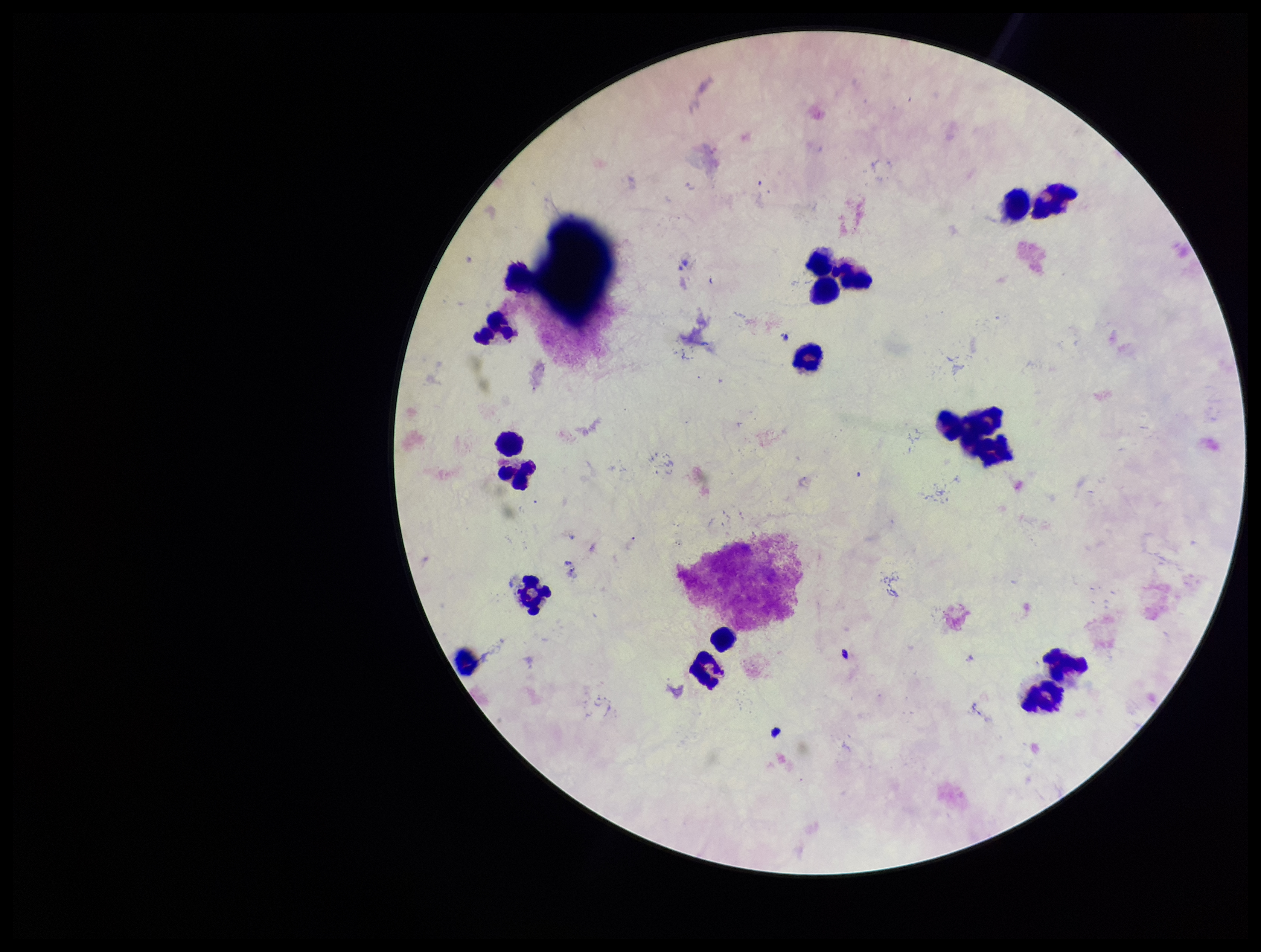
Summary:
  - Stain: Giemsa
  - Plasmodium parasites: none identified
  - Parasite count: 0
  - Capture: smartphone photograph through the microscope eyepiece
  - Species reported for this patient: Plasmodium falciparum
  - Preparation: thick
  - Image size: 1261×952 pixels
  - Field of view: one from this slide
  - Leukocyte count: 17
  - Patient malaria status: positive